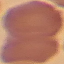

Summary:
  - Result: negative for malaria parasites
  - Preparation: thin blood film
  - Stain: Giemsa
  - Image type: automatically extracted cell patch, resized to 64 × 64 pixels
  - Capture: smartphone camera at the microscope eyepiece